State which cell type is depicted.
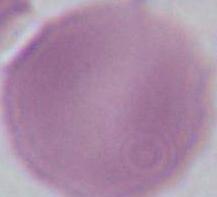
This is an erythrocyte.

Micrograph. Captured at 1000x magnification.